Give the position of every malaria parasite.
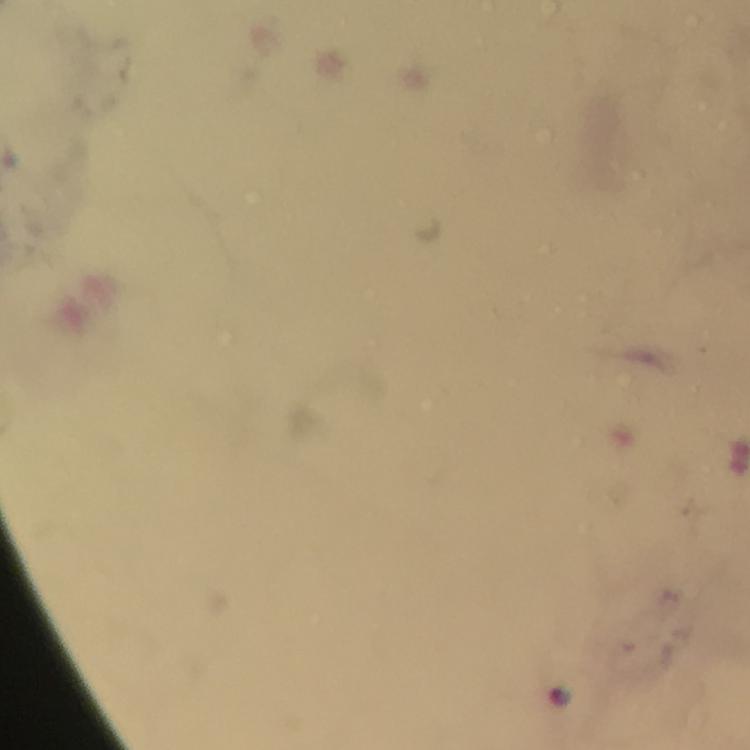

Approximate centers as {x, y} in pixels.
Malaria parasites: {560, 694}.

capture = smartphone photograph through a microscope
preparation = thick blood smear
immersion oil = applied
context = from a diagnostic examination for malaria
cropped from = a single field of view
stain = Giemsa
magnification = 100x
image size = 750×750 pixels